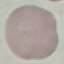

Result: no malaria parasites detected. Acquired by smartphone through the microscope eyepiece. Cell patch, automatically extracted from a larger field of view and resized to 64 × 64 pixels. Giemsa-stained preparation. Thin blood film.